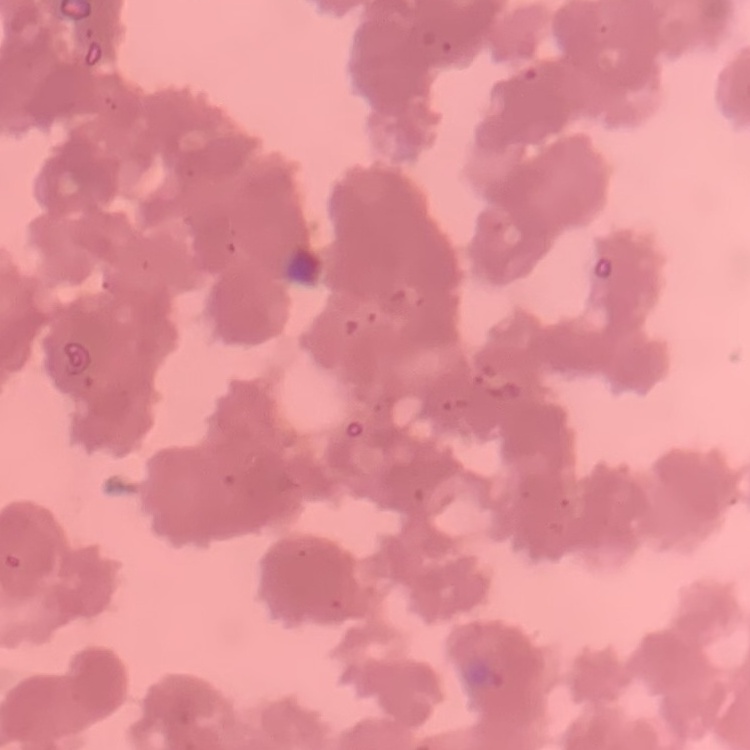

The red blood cells exhibit rouleaux formation. Square crop of a larger photomicrograph. Thin blood film. Field's or Giemsa stain.